Outline each blood parasite and name the species.
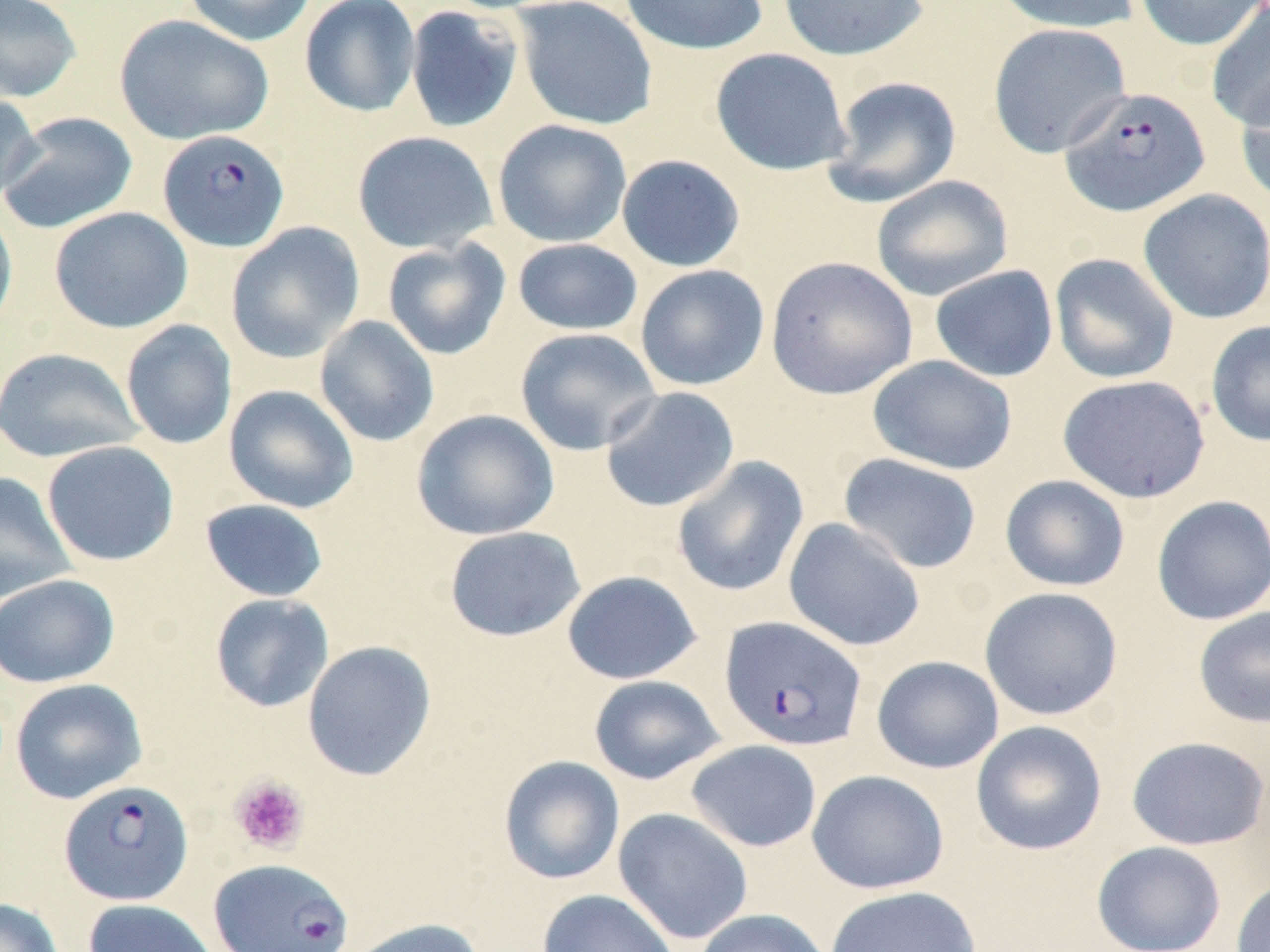
Approximate bounding boxes as [x1, y1, x2, y2] in pixels.
Plasmodium falciparum-infected red blood cells: [1060, 86, 1211, 217], [157, 129, 290, 252], [720, 616, 867, 751], [58, 779, 194, 906], [208, 858, 354, 951].
No Plasmodium ovale, Plasmodium malariae, Plasmodium vivax, Babesia divergens, or Trypanosoma brucei observed.

Uninfected red blood cell locations: [0, 0, 83, 104], [180, 0, 319, 46], [513, 0, 658, 131], [619, 0, 770, 55], [777, 0, 930, 61], [991, 0, 1141, 34], [1135, 0, 1266, 51], [299, 1, 422, 118], [1206, 3, 1270, 132], [403, 5, 523, 134], [114, 14, 274, 145], [988, 22, 1131, 158], [710, 47, 853, 176], [823, 76, 962, 207], [1236, 79, 1270, 208], [0, 90, 42, 205], [0, 111, 138, 235], [492, 119, 632, 248], [351, 130, 498, 254], [616, 154, 745, 272], [871, 175, 1013, 302], [1137, 188, 1270, 324], [0, 202, 18, 337], [49, 207, 193, 334], [225, 222, 365, 363], [382, 238, 512, 360], [512, 238, 643, 336], [1049, 253, 1180, 384], [765, 256, 917, 400], [635, 265, 769, 391], [930, 265, 1059, 382], [314, 315, 440, 447], [120, 319, 237, 450], [1205, 319, 1270, 447], [515, 327, 661, 456], [0, 347, 143, 463], [868, 355, 1018, 475], [1057, 374, 1211, 504], [223, 384, 359, 513], [600, 386, 740, 513], [411, 409, 560, 541], [41, 440, 179, 567], [838, 453, 982, 574], [671, 455, 809, 597], [0, 472, 77, 604], [1000, 474, 1130, 592], [1151, 495, 1270, 626], [200, 498, 330, 602], [784, 517, 925, 651], [443, 526, 585, 642], [561, 570, 702, 684], [0, 574, 120, 688], [979, 587, 1123, 721], [209, 592, 334, 713], [1193, 605, 1270, 729], [302, 640, 436, 781], [871, 655, 1004, 774], [588, 675, 726, 785], [10, 678, 147, 805], [970, 720, 1108, 856], [1126, 736, 1269, 850], [685, 740, 822, 852], [497, 755, 625, 885], [807, 769, 950, 894], [613, 807, 754, 945], [1091, 840, 1227, 952], [1230, 878, 1270, 952], [824, 885, 981, 952], [537, 888, 679, 952], [0, 897, 65, 952], [82, 898, 223, 952], [692, 908, 833, 952], [343, 917, 486, 952]. Platelet locations: [229, 776, 310, 855]. Slide-level diagnosis: Plasmodium falciparum. Image is 1270×952 pixels. One field of a larger specimen. Thin blood film. Light microscopy. May-Grünwald-Giemsa stain. Captured at 1000x magnification.